Identify the parasite.
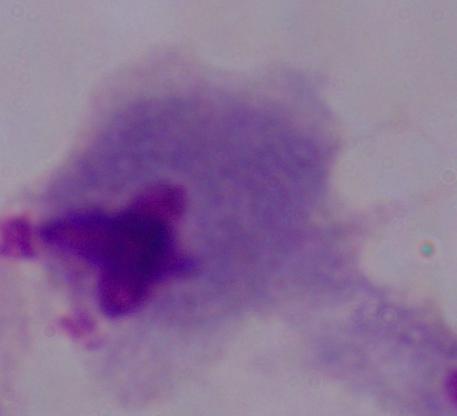
A trichomonad.

Summary:
  - Magnification: 1000x
  - Modality: photomicrograph